Classify this cell by malaria status.
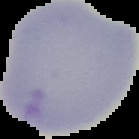
It is uninfected.

{
  "image_size": "139×139 pixels",
  "preparation": "thin blood film",
  "image_type": "cell region segmented out of the field of view; surrounding area masked to black"
}